Identify the parasite.
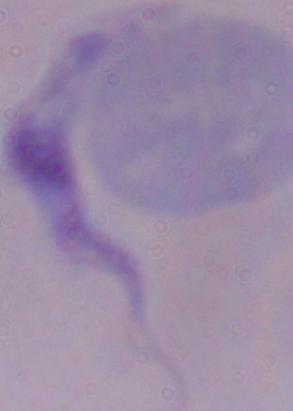
This is a trypanosome.

Photomicrograph. Captured at 1000x magnification.